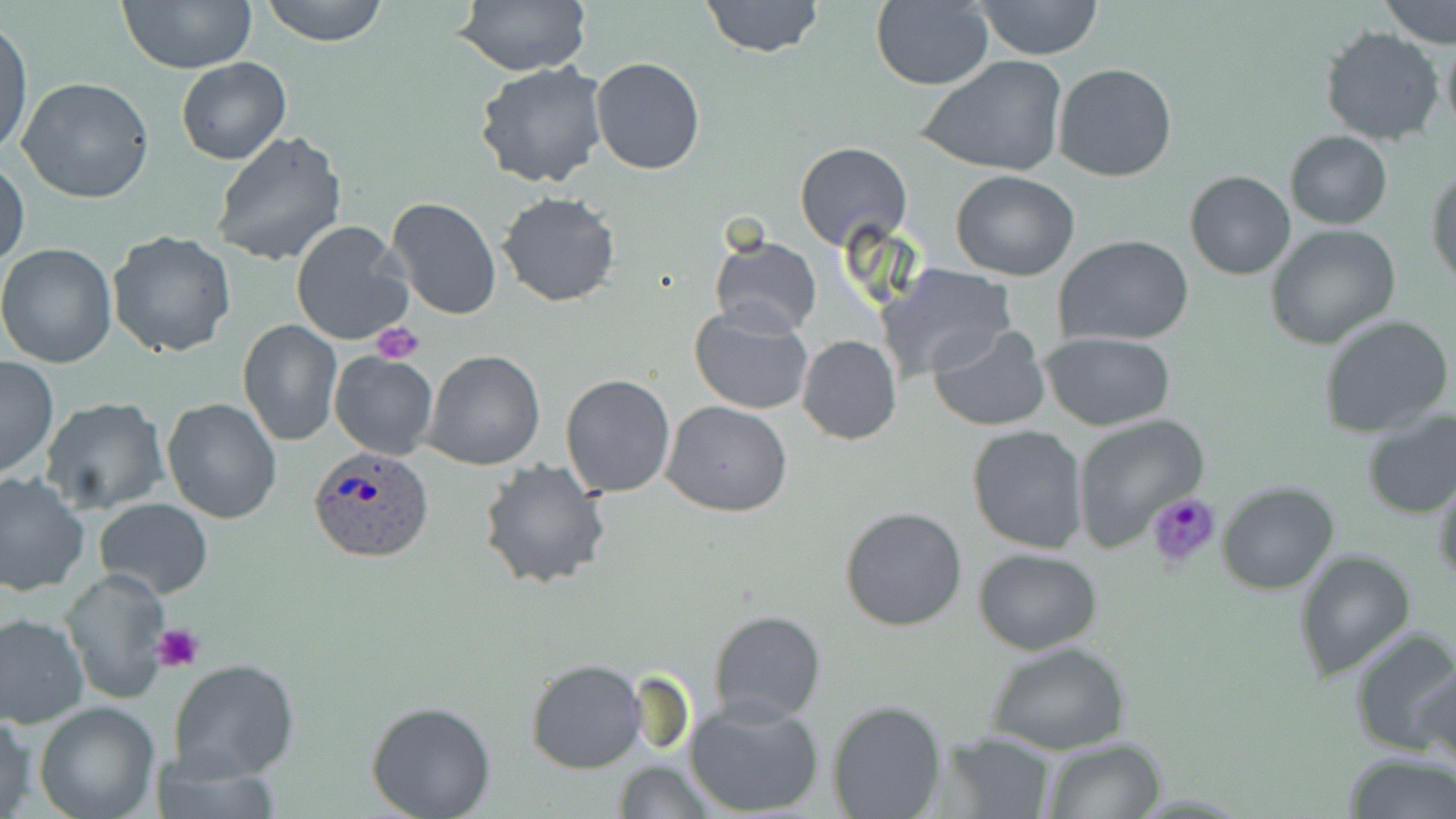
Approximate bounding boxes as (x1,y1)-(x2,y2) corner pairs in pixels. Uninfected red blood cell locations: (117,0)-(259,73), (259,0)-(390,46), (453,0)-(591,76), (699,0)-(825,56), (1381,0)-(1455,48), (869,1)-(994,89), (970,1)-(1105,59), (0,19)-(33,160), (1320,26)-(1447,146), (1439,31)-(1456,140), (917,55)-(1070,179), (591,56)-(706,175), (175,57)-(292,165), (473,61)-(609,190), (1054,63)-(1177,183), (18,78)-(156,204), (1285,129)-(1393,230), (211,130)-(348,268), (794,141)-(913,252), (1,158)-(28,269), (1427,165)-(1456,290), (950,170)-(1079,280), (1184,170)-(1296,279), (497,192)-(622,308), (385,197)-(502,320), (289,222)-(415,345), (1265,225)-(1401,349), (107,230)-(237,358), (709,235)-(822,337), (1054,236)-(1193,347), (0,243)-(120,367), (880,264)-(1016,381), (689,305)-(816,416), (1317,313)-(1453,438), (237,319)-(342,445), (928,324)-(1053,433), (1041,332)-(1176,431), (797,335)-(901,445), (422,350)-(546,470), (328,351)-(441,460), (0,357)-(58,481), (560,373)-(676,499), (39,396)-(170,514), (161,398)-(283,524), (660,401)-(792,517), (1359,407)-(1456,517), (1070,413)-(1208,551), (966,425)-(1088,554), (477,458)-(613,592), (1432,469)-(1456,588), (0,471)-(90,595), (1217,480)-(1340,595), (94,497)-(213,597), (839,506)-(968,630), (974,547)-(1104,655), (1293,548)-(1416,682), (59,571)-(172,704), (707,608)-(829,725), (0,613)-(89,727), (1347,626)-(1456,757), (984,640)-(1133,754), (170,657)-(301,783), (525,659)-(646,773), (1414,664)-(1456,775), (682,696)-(827,819), (825,699)-(947,818), (364,700)-(497,819), (34,701)-(162,819), (0,708)-(38,818), (938,732)-(1057,818), (1040,737)-(1167,818), (1342,751)-(1455,819), (611,760)-(716,817). Plasmodium ovale-infected red blood cell locations: (310,448)-(437,566). Platelet locations: (372,323)-(425,364), (153,622)-(206,676). Slide-level diagnosis: Plasmodium ovale. May-Grünwald-Giemsa-stained preparation. Captured at 1000x magnification. Optical microscopy. Thin blood film. Image is 1456×819 pixels. Single field of view.